Report the malaria status of this cell.
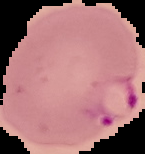
It is parasitized.

Cell region segmented out of the field of view; the surrounding area is masked to black. From a thin blood smear. Image is 145×154 pixels.